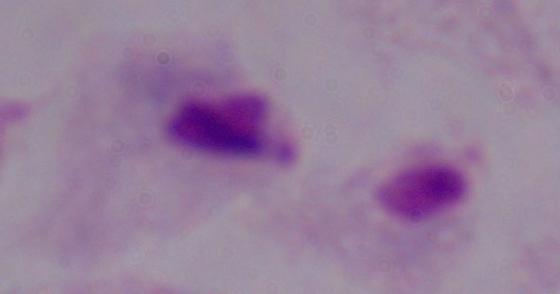
Summary:
  - Magnification: 1000x
  - Modality: micrograph
  - Identification: trichomonad